Describe the morphology of the erythrocytes.
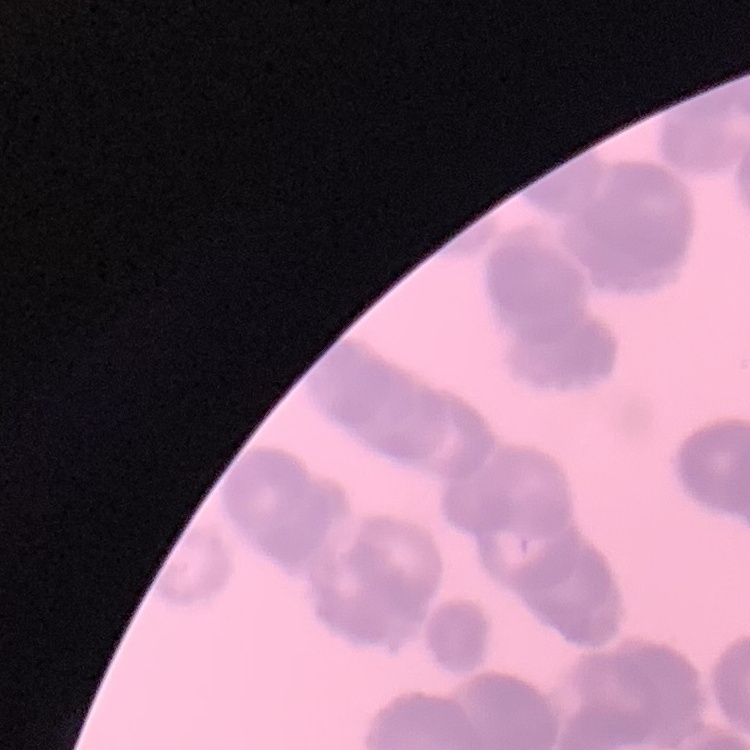

Rouleaux formation.

Thin blood film. One tile cut from a larger photomicrograph. Field's or Giemsa stain.